Assess for malaria.
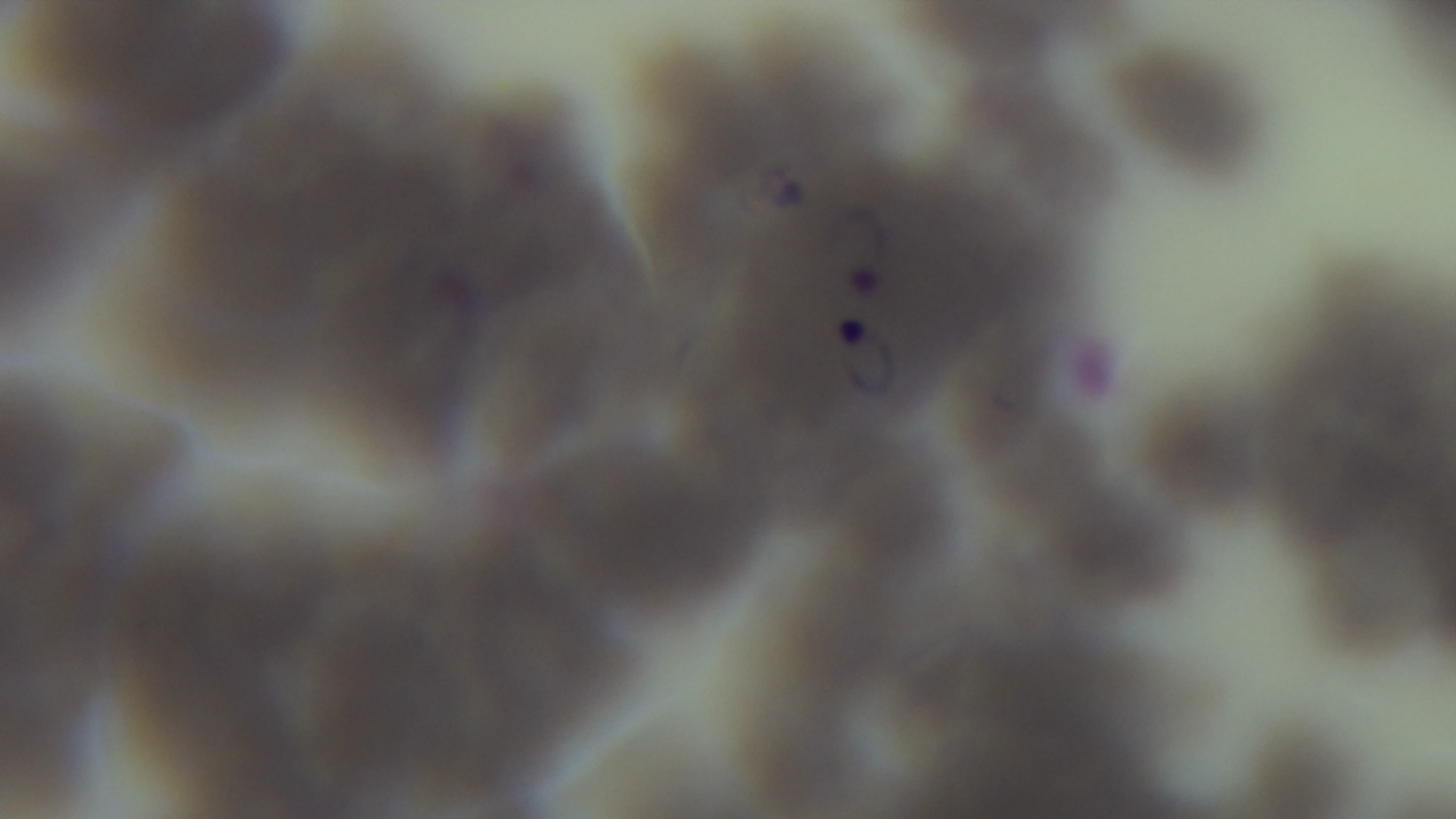
Infected.

Summary:
  - Modality: light microscopy
  - Field of view: single
  - Capture: mounted 4K digital camera
  - Objective: 100x oil immersion
  - Stain: Giemsa
  - Preparation: thin